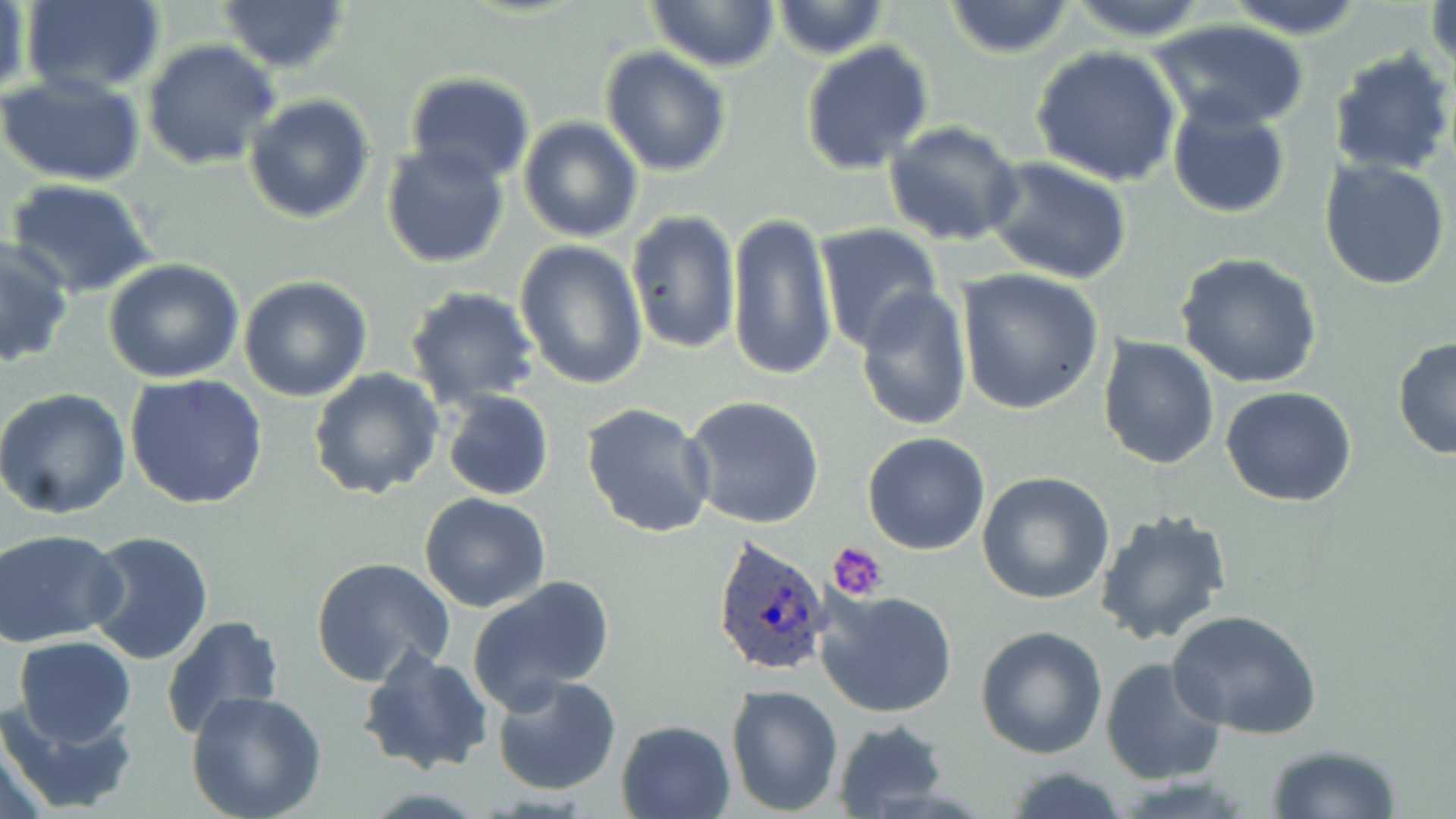

slide-level diagnosis = Plasmodium ovale
preparation = thin blood smear
Plasmodium ovale-infected red blood cell locations = approximate bounding boxes as (x1, y1, x2, y2) in pixels: (710, 535, 835, 678)
field of view = one of a larger specimen
modality = optical microscopy
image size = 1456×819 pixels
magnification = 1000x
stain = May-Grünwald-Giemsa
platelet locations = approximate bounding boxes as (x1, y1, x2, y2) in pixels: (829, 542, 890, 602)
uninfected red blood cell locations = approximate bounding boxes as (x1, y1, x2, y2) in pixels: (20, 0, 166, 96), (218, 0, 351, 73), (646, 0, 779, 73), (1219, 0, 1370, 37), (1426, 0, 1455, 80), (771, 1, 889, 58), (942, 1, 1078, 59), (1062, 1, 1213, 42), (2, 3, 34, 106), (1148, 18, 1311, 131), (142, 40, 281, 171), (800, 41, 935, 176), (1030, 45, 1182, 187), (599, 46, 731, 176), (1327, 48, 1455, 178), (403, 72, 536, 187), (0, 73, 146, 187), (243, 93, 375, 224), (1166, 100, 1291, 217), (518, 116, 644, 243), (883, 121, 1025, 248), (380, 142, 511, 267), (984, 156, 1134, 285), (1318, 156, 1453, 290), (4, 177, 159, 298), (626, 210, 741, 358), (726, 210, 835, 382), (816, 224, 945, 354), (0, 240, 73, 367), (513, 240, 648, 390), (1177, 254, 1322, 390), (102, 260, 246, 384), (956, 270, 1106, 415), (239, 275, 372, 402), (404, 285, 541, 409), (855, 285, 973, 431), (1097, 335, 1220, 470), (1392, 337, 1455, 461), (308, 368, 443, 502), (125, 373, 268, 509), (1220, 385, 1357, 507), (0, 388, 133, 519), (442, 390, 553, 502), (683, 395, 825, 530), (581, 402, 717, 539), (862, 432, 991, 556), (976, 473, 1116, 607), (419, 492, 551, 612), (1094, 508, 1233, 649), (0, 528, 127, 646), (83, 529, 217, 666), (311, 556, 456, 688), (467, 576, 616, 709), (816, 588, 958, 719), (1166, 610, 1322, 738), (160, 614, 286, 741), (977, 624, 1108, 759), (13, 636, 137, 747), (358, 647, 493, 775), (1099, 657, 1226, 786), (491, 673, 623, 794), (725, 683, 845, 815), (185, 691, 327, 819), (0, 694, 140, 816), (615, 718, 738, 819), (832, 719, 951, 817), (0, 721, 55, 819), (1265, 743, 1401, 818), (1000, 763, 1133, 819)